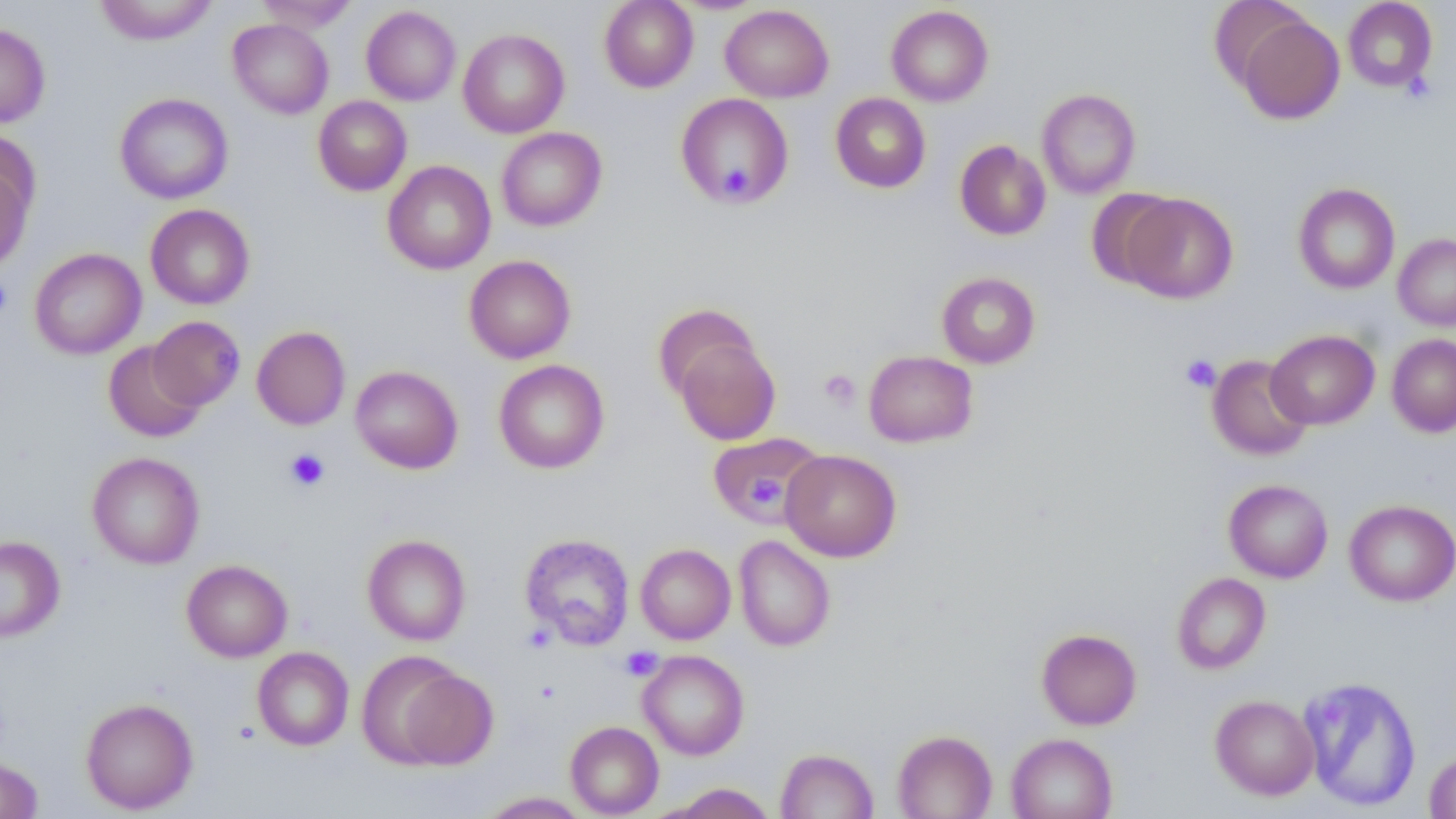 Approximate bounding boxes as named x1/y1/x2/y2 corners in pixels. Platelet locations: (x1=1400, y1=71, x2=1435, y2=104), (x1=714, y1=161, x2=759, y2=204), (x1=0, y1=277, x2=12, y2=320), (x1=1180, y1=354, x2=1221, y2=393), (x1=819, y1=369, x2=860, y2=410), (x1=285, y1=448, x2=330, y2=492), (x1=741, y1=470, x2=792, y2=511), (x1=620, y1=647, x2=663, y2=681). Uninfected red blood cell locations: (x1=94, y1=0, x2=219, y2=45), (x1=256, y1=0, x2=360, y2=33), (x1=599, y1=0, x2=698, y2=92), (x1=1343, y1=0, x2=1437, y2=92), (x1=720, y1=4, x2=834, y2=103), (x1=361, y1=5, x2=461, y2=105), (x1=885, y1=5, x2=994, y2=107), (x1=1236, y1=14, x2=1345, y2=125), (x1=228, y1=18, x2=333, y2=119), (x1=0, y1=23, x2=50, y2=128), (x1=457, y1=28, x2=570, y2=138), (x1=1037, y1=88, x2=1141, y2=198), (x1=115, y1=92, x2=233, y2=204), (x1=830, y1=92, x2=931, y2=193), (x1=675, y1=93, x2=794, y2=208), (x1=313, y1=95, x2=412, y2=196), (x1=496, y1=127, x2=607, y2=231), (x1=0, y1=128, x2=40, y2=228), (x1=954, y1=140, x2=1051, y2=240), (x1=382, y1=160, x2=496, y2=275), (x1=0, y1=166, x2=33, y2=271), (x1=1292, y1=183, x2=1400, y2=294), (x1=1086, y1=189, x2=1181, y2=289), (x1=1122, y1=193, x2=1238, y2=304), (x1=145, y1=204, x2=255, y2=309), (x1=1393, y1=233, x2=1456, y2=330), (x1=29, y1=248, x2=146, y2=359), (x1=464, y1=255, x2=576, y2=363), (x1=936, y1=271, x2=1041, y2=368), (x1=653, y1=304, x2=760, y2=401), (x1=147, y1=315, x2=244, y2=410), (x1=251, y1=325, x2=350, y2=430), (x1=1266, y1=329, x2=1379, y2=429), (x1=1386, y1=333, x2=1456, y2=437), (x1=673, y1=336, x2=781, y2=445), (x1=104, y1=342, x2=206, y2=442), (x1=863, y1=350, x2=978, y2=448), (x1=1207, y1=354, x2=1313, y2=461), (x1=493, y1=359, x2=609, y2=473), (x1=350, y1=365, x2=463, y2=473), (x1=707, y1=433, x2=823, y2=526), (x1=780, y1=449, x2=901, y2=561), (x1=87, y1=451, x2=205, y2=569), (x1=1223, y1=478, x2=1333, y2=583), (x1=1344, y1=499, x2=1456, y2=606), (x1=362, y1=533, x2=471, y2=645), (x1=519, y1=533, x2=635, y2=650), (x1=733, y1=535, x2=835, y2=651), (x1=0, y1=536, x2=65, y2=643), (x1=635, y1=543, x2=736, y2=644), (x1=181, y1=559, x2=292, y2=661), (x1=1172, y1=572, x2=1271, y2=674), (x1=1036, y1=628, x2=1142, y2=730), (x1=252, y1=647, x2=354, y2=750), (x1=638, y1=650, x2=749, y2=760), (x1=356, y1=651, x2=468, y2=768), (x1=396, y1=668, x2=498, y2=770), (x1=1298, y1=676, x2=1421, y2=812), (x1=1210, y1=695, x2=1320, y2=799), (x1=80, y1=697, x2=198, y2=814), (x1=565, y1=721, x2=664, y2=817), (x1=892, y1=729, x2=997, y2=819), (x1=1006, y1=733, x2=1117, y2=819), (x1=775, y1=747, x2=879, y2=818), (x1=1424, y1=748, x2=1456, y2=818), (x1=0, y1=757, x2=43, y2=818), (x1=661, y1=782, x2=778, y2=818), (x1=478, y1=791, x2=590, y2=818). Slide-level diagnosis: negative for blood parasites. Captured at 1000x magnification. Single field of view. Image is 1456×819 pixels. Light microscopy. May-Grünwald-Giemsa stain. Thin blood smear.